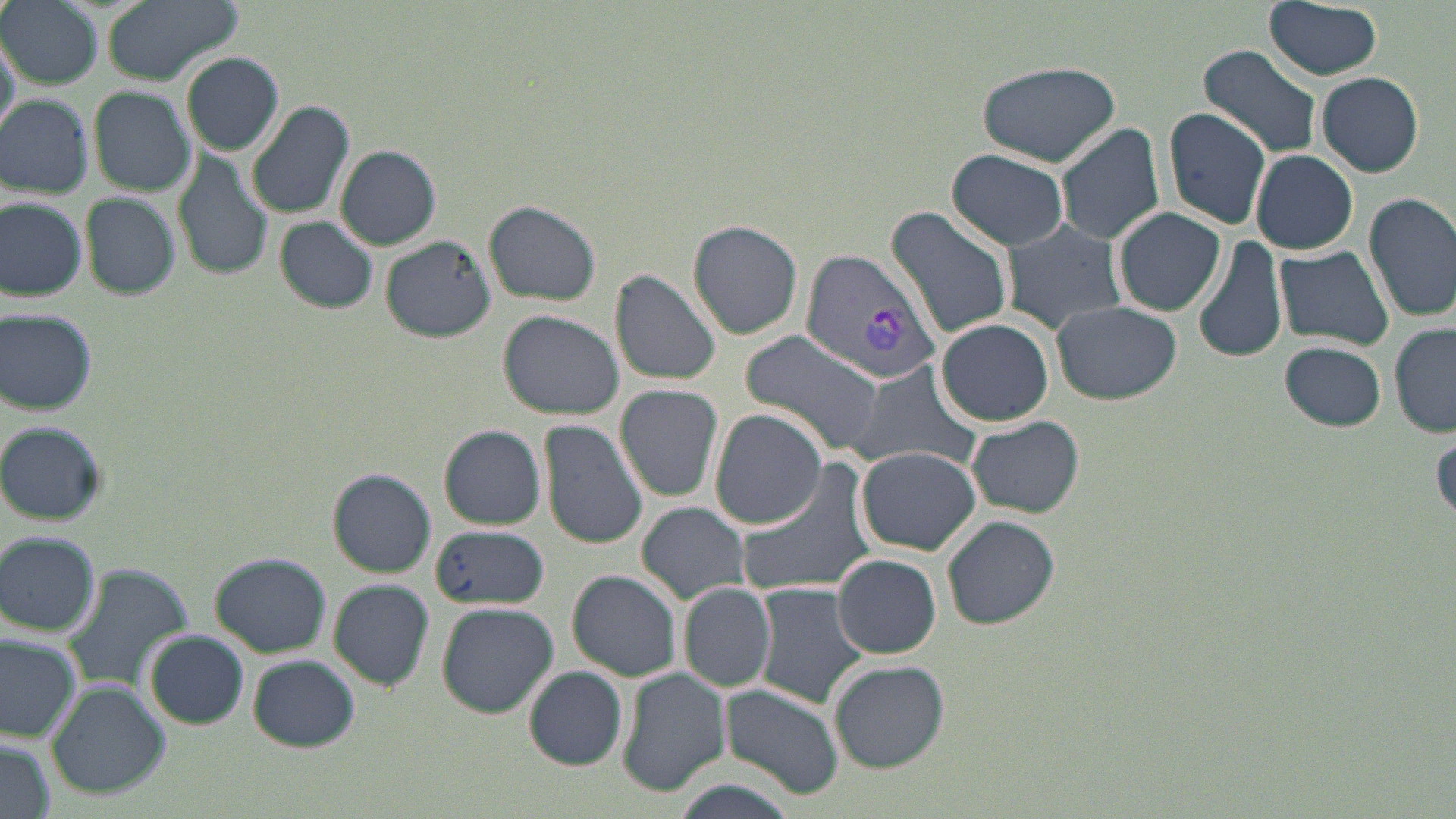

slide_level_diagnosis: Plasmodium vivax
field_of_view: single
modality: optical microscopy
image_size: 1456×819 pixels
plasmodium_vivax_infected_red_blood_cell_locations: 'approximate bounding boxes as [x1, y1, x2, y2] in pixels: [802, 249, 944, 389]'
magnification: 1000x
preparation: thin blood film
stain: May-Grünwald-Giemsa
uninfected_red_blood_cell_locations: 'approximate bounding boxes as [x1, y1, x2, y2] in pixels: [0, 0, 103, 88], [99, 0, 244, 86], [1262, 0, 1384, 80], [1, 34, 21, 133], [1197, 42, 1322, 161], [182, 51, 284, 154], [972, 59, 1124, 166], [1316, 72, 1424, 176], [88, 86, 194, 196], [0, 94, 93, 197], [246, 101, 354, 220], [1159, 107, 1272, 229], [1054, 123, 1166, 246], [172, 145, 274, 282], [335, 145, 442, 249], [947, 149, 1071, 249], [1251, 150, 1358, 255], [80, 191, 181, 301], [1362, 191, 1456, 321], [0, 195, 88, 301], [483, 200, 600, 306], [883, 208, 1015, 340], [1112, 208, 1225, 316], [274, 217, 380, 314], [687, 219, 804, 340], [1001, 220, 1130, 334], [380, 236, 496, 343], [1193, 236, 1289, 366], [1273, 245, 1394, 350], [611, 269, 724, 386], [1051, 300, 1181, 404], [0, 307, 97, 414], [498, 308, 623, 420], [935, 318, 1056, 426], [1390, 323, 1456, 439], [744, 333, 887, 458], [1279, 341, 1388, 430], [854, 362, 982, 473], [615, 384, 725, 502], [712, 409, 828, 530], [965, 415, 1084, 518], [537, 418, 649, 549], [0, 422, 106, 524], [439, 425, 547, 530], [1430, 425, 1455, 523], [856, 446, 984, 556], [730, 458, 879, 600], [329, 470, 435, 577], [637, 502, 752, 603], [942, 514, 1061, 629], [427, 523, 551, 609], [1, 531, 101, 637], [832, 552, 942, 659], [211, 553, 329, 657], [62, 561, 195, 694], [566, 569, 683, 682], [328, 579, 436, 690], [753, 580, 872, 709], [678, 581, 778, 693], [436, 602, 558, 718], [143, 629, 250, 730], [0, 632, 81, 741], [245, 654, 362, 752], [829, 658, 949, 772], [524, 666, 628, 768], [617, 667, 731, 796], [45, 684, 170, 798], [720, 684, 845, 798], [0, 736, 57, 819]'